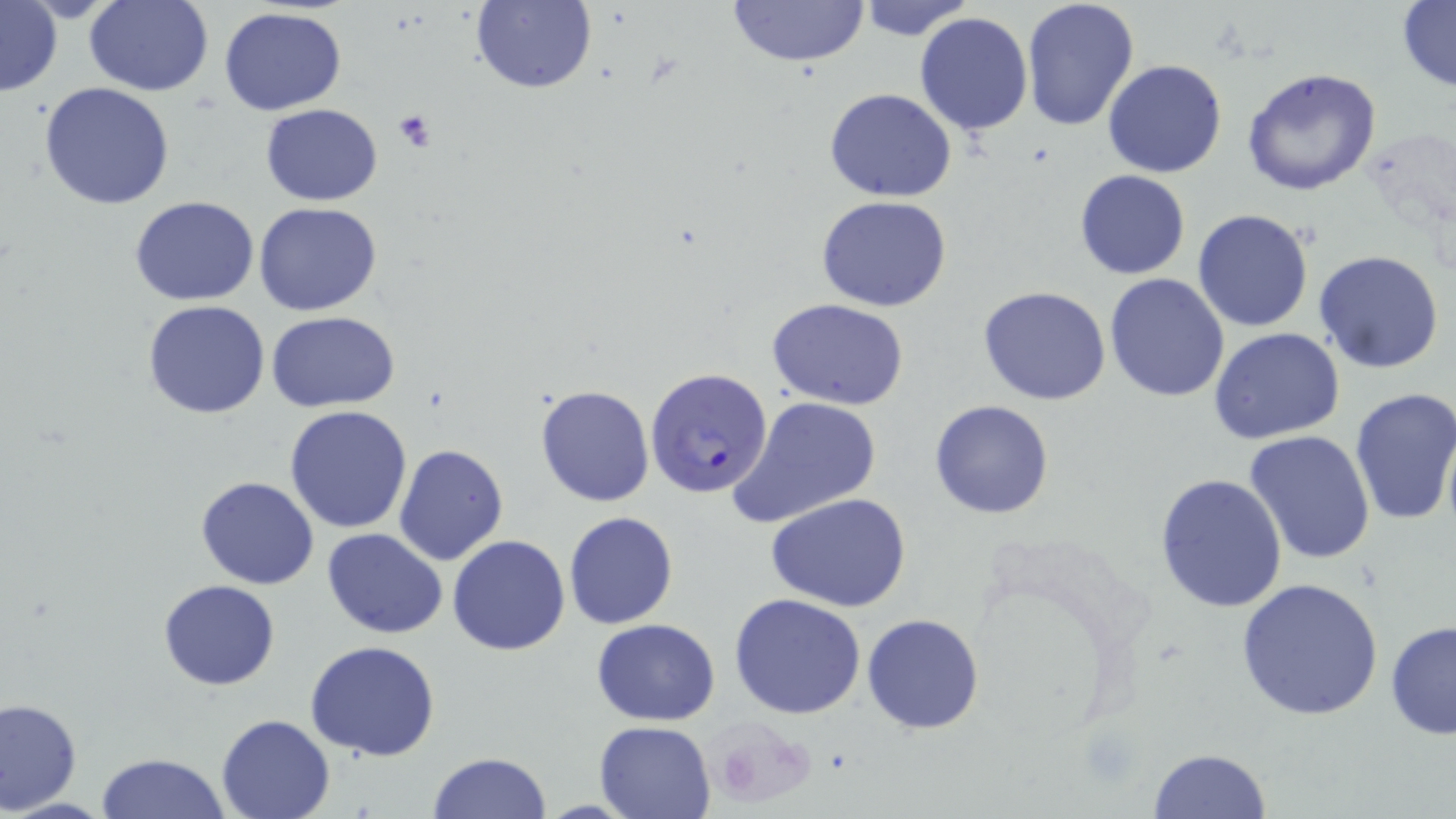
slide-level diagnosis = Plasmodium falciparum
stain = May-Grünwald-Giemsa
uninfected red blood cell locations = approximate bounding boxes as [x1, y1, x2, y2] in pixels: [84, 0, 214, 95], [725, 0, 871, 67], [472, 1, 598, 94], [854, 1, 979, 42], [1020, 1, 1142, 134], [0, 2, 62, 98], [1396, 2, 1456, 91], [219, 7, 347, 114], [914, 12, 1033, 137], [1103, 58, 1227, 177], [1241, 67, 1384, 197], [39, 82, 176, 211], [825, 89, 957, 202], [261, 104, 383, 204], [1074, 168, 1191, 280], [816, 194, 953, 312], [131, 196, 261, 306], [254, 201, 382, 316], [1192, 209, 1314, 332], [1313, 250, 1445, 374], [1103, 273, 1231, 402], [978, 286, 1113, 405], [765, 297, 910, 410], [143, 300, 271, 419], [268, 311, 399, 410], [1209, 328, 1347, 444], [534, 384, 656, 507], [1348, 386, 1456, 526], [728, 396, 882, 529], [929, 400, 1055, 519], [285, 405, 415, 534], [1244, 430, 1376, 567], [393, 444, 509, 566], [1156, 471, 1289, 615], [195, 476, 319, 590], [765, 490, 912, 612], [563, 511, 678, 630], [323, 528, 449, 638], [447, 535, 572, 656], [1236, 577, 1384, 722], [158, 579, 280, 690], [728, 594, 867, 720], [863, 613, 984, 734], [591, 618, 722, 725], [1385, 618, 1456, 741], [304, 639, 443, 760], [0, 697, 82, 815], [216, 714, 336, 819], [592, 720, 717, 818], [1148, 746, 1274, 818], [97, 752, 231, 819], [427, 752, 551, 819]
preparation = thin blood smear
magnification = 1000x
platelet locations = approximate bounding boxes as [x1, y1, x2, y2] in pixels: [392, 110, 439, 152], [712, 724, 801, 802]
image size = 1456×819 pixels
modality = optical microscopy
Plasmodium falciparum-infected red blood cell locations = approximate bounding boxes as [x1, y1, x2, y2] in pixels: [646, 368, 776, 500]
field of view = one of a larger specimen